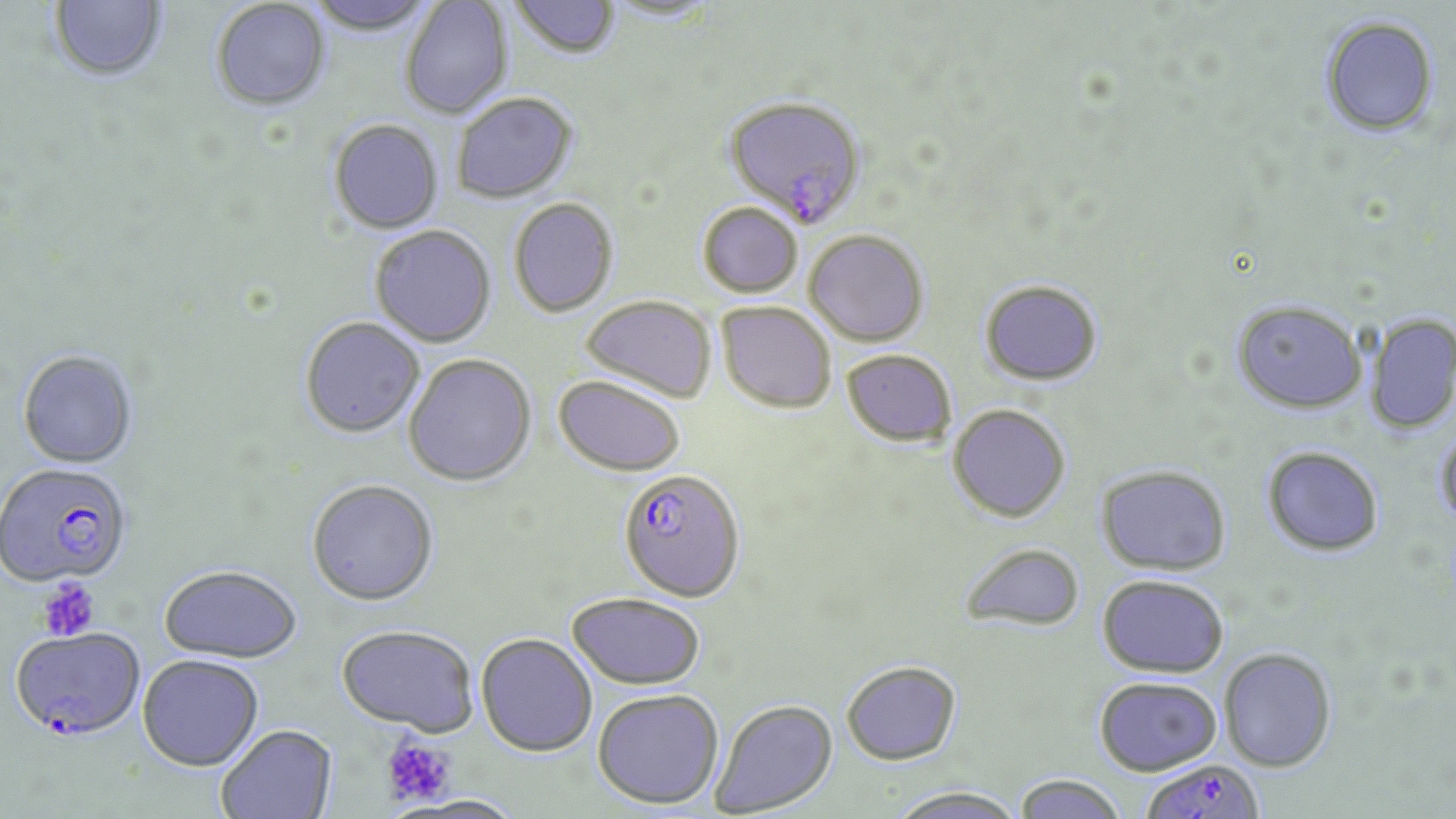

Approximate bounding boxes as [x1, y1, x2, y2] in pixels. Plasmodium falciparum-infected red blood cell locations: [723, 94, 868, 225], [0, 465, 134, 590], [617, 467, 746, 602], [11, 629, 147, 743], [1144, 759, 1271, 819]. Platelet locations: [37, 578, 100, 641], [381, 735, 455, 807]. Uninfected red blood cell locations: [49, 0, 168, 83], [305, 0, 437, 36], [400, 0, 513, 120], [510, 0, 621, 59], [601, 0, 722, 23], [210, 1, 331, 112], [1319, 15, 1440, 137], [451, 92, 577, 203], [329, 119, 443, 234], [509, 198, 618, 317], [698, 201, 803, 297], [369, 225, 497, 347], [804, 229, 929, 345], [980, 279, 1102, 386], [580, 295, 717, 401], [1232, 299, 1367, 414], [716, 301, 837, 413], [1365, 313, 1456, 435], [299, 316, 424, 438], [841, 349, 957, 446], [17, 351, 138, 470], [404, 354, 536, 486], [553, 375, 685, 477], [948, 404, 1071, 522], [1434, 426, 1456, 534], [1262, 446, 1384, 556], [1096, 464, 1232, 575], [306, 479, 439, 606], [957, 542, 1086, 632], [159, 565, 302, 663], [1097, 575, 1229, 677], [566, 591, 706, 689], [336, 624, 480, 736], [476, 633, 598, 756], [1219, 648, 1337, 771], [137, 655, 264, 772], [840, 660, 962, 765], [1094, 676, 1222, 775], [592, 688, 725, 809], [709, 698, 839, 817], [216, 725, 338, 819], [1012, 773, 1128, 819], [886, 785, 1028, 819], [398, 795, 532, 819]. Slide-level diagnosis: Plasmodium falciparum. Thin blood film. Captured at 1000x magnification. May-Grünwald-Giemsa-stained preparation. Single field of view. Light microscopy. Image is 1456×819 pixels.